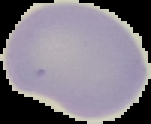 Result: no malaria parasites seen. Image is 151×124 pixels. From a thin blood film. The area outside the segmented cell region is set to black.